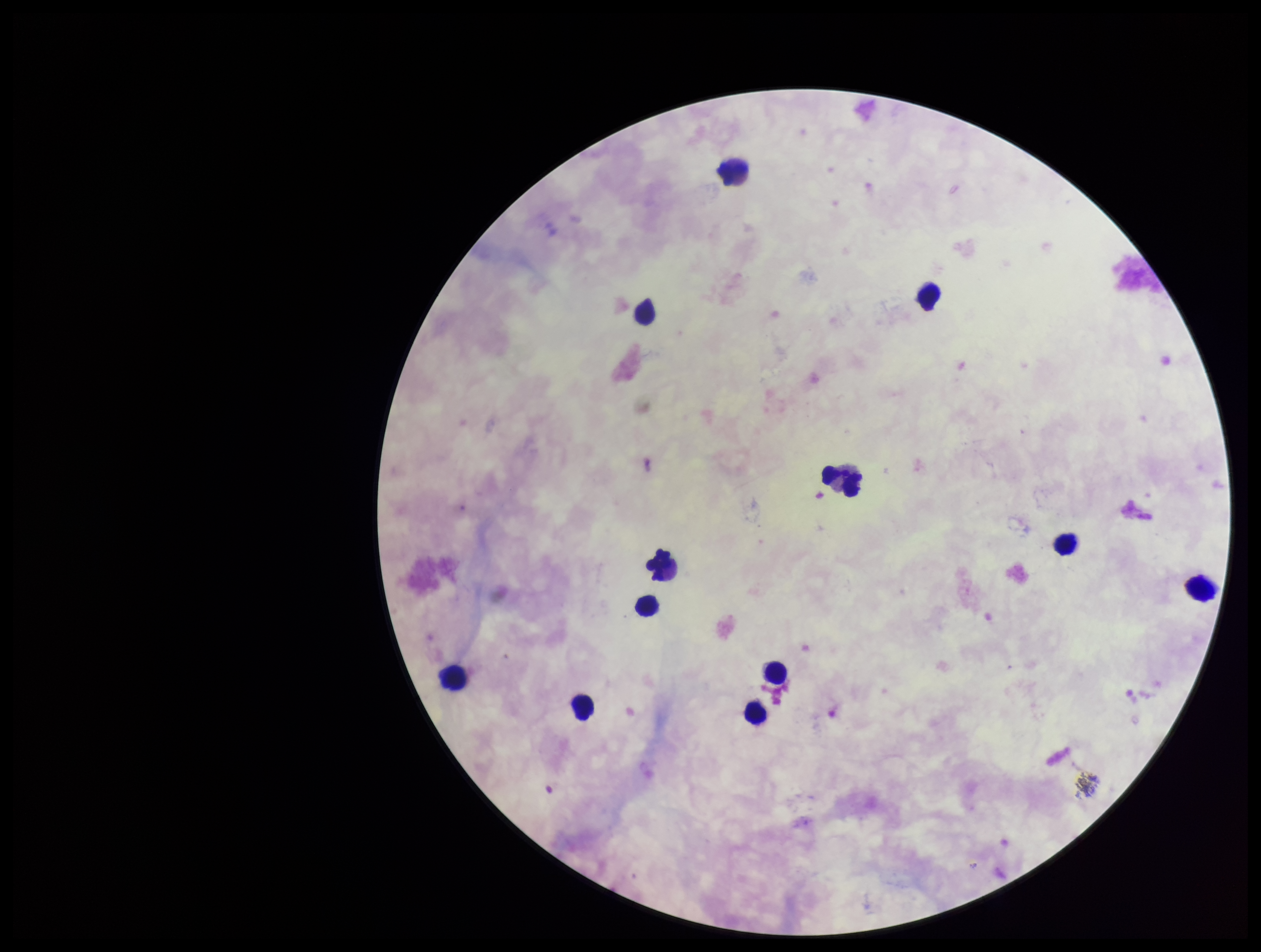

Summary:
  - Patient malaria status: negative
  - Field of view: one from this slide
  - Capture: smartphone photograph through the microscope eyepiece
  - Image size: 1261×952 pixels
  - Stain: Giemsa
  - Plasmodium parasites: none detected
  - Leukocyte count: 12
  - Parasite count: 0
  - Preparation: thick